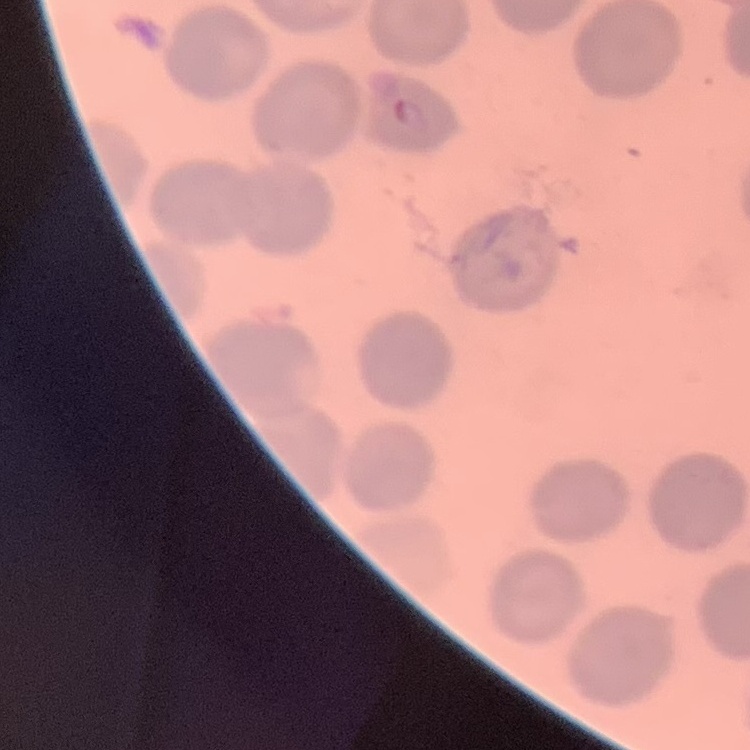

The erythrocytes show no rouleaux formation. Thin blood smear. Square crop of a larger photomicrograph. Stained with either Field's or Giemsa.